Classify this cell by malaria status.
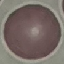

Uninfected.

Summary:
  - Preparation: thin smear
  - Image type: cell patch, automatically extracted from a larger field of view and resized to 64 × 64 pixels
  - Capture: smartphone camera at the microscope eyepiece
  - Stain: Giemsa